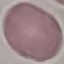
Result: no malaria parasites detected. Thin blood film. Cell patch, automatically extracted from a larger field of view and resized to 64 × 64 pixels. Giemsa-stained preparation. Acquired by smartphone through the microscope eyepiece.